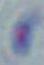

identification = Toxoplasma gondii
modality = photomicrograph
magnification = 1000x